Locate platelets.
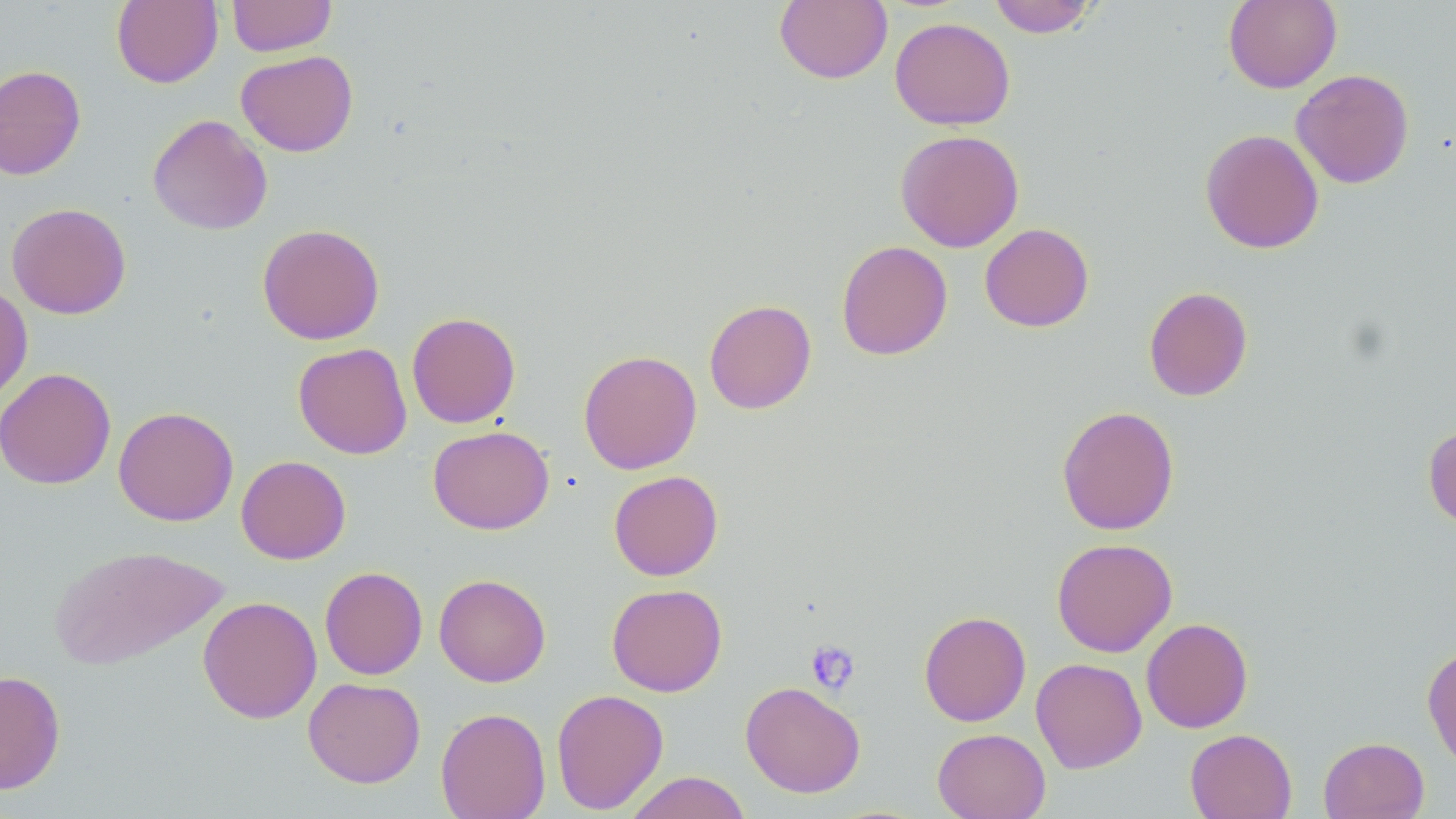
Approximate bounding boxes as [x1, y1, x2, y2] in pixels.
Platelets: [805, 640, 861, 695].

Uninfected red blood cell locations: [111, 0, 223, 88], [226, 0, 337, 56], [774, 0, 892, 84], [987, 0, 1099, 38], [1223, 0, 1342, 93], [889, 16, 1015, 131], [235, 50, 358, 157], [0, 64, 86, 180], [1290, 68, 1414, 189], [148, 114, 273, 235], [1200, 128, 1324, 254], [895, 129, 1024, 252], [6, 202, 131, 319], [257, 223, 385, 345], [979, 223, 1094, 332], [836, 240, 953, 360], [0, 282, 33, 407], [1144, 285, 1253, 401], [704, 299, 817, 414], [406, 312, 521, 428], [293, 342, 412, 459], [578, 350, 702, 474], [0, 367, 116, 489], [1056, 405, 1180, 535], [113, 406, 238, 526], [1423, 424, 1456, 531], [428, 425, 554, 535], [236, 455, 351, 564], [609, 470, 723, 581], [1051, 537, 1178, 657], [50, 544, 229, 670], [319, 566, 428, 680], [434, 573, 551, 687], [606, 583, 727, 697], [197, 595, 322, 724], [918, 610, 1031, 727], [1141, 617, 1253, 733], [1422, 644, 1456, 772], [1031, 657, 1147, 773], [0, 670, 66, 795], [303, 676, 426, 788], [740, 681, 865, 797], [551, 688, 669, 814], [435, 707, 551, 819], [932, 728, 1051, 819], [1185, 728, 1297, 819], [1318, 736, 1430, 819], [624, 771, 753, 819]. Slide-level diagnosis: no evidence of blood parasites. Captured at 1000x magnification. Light microscopy. Thin blood smear. One field of a larger specimen. Image is 1456×819 pixels. May-Grünwald-Giemsa-stained preparation.